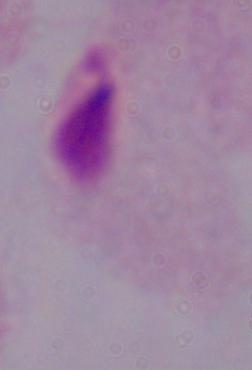

modality = micrograph
magnification = 1000x
identification = trichomonad